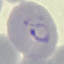
Result: malaria parasites detected. Giemsa-stained preparation. Thin blood smear. Automatically extracted cell patch, resized to 64 × 64 pixels. Photographed with a smartphone camera at the microscope eyepiece.